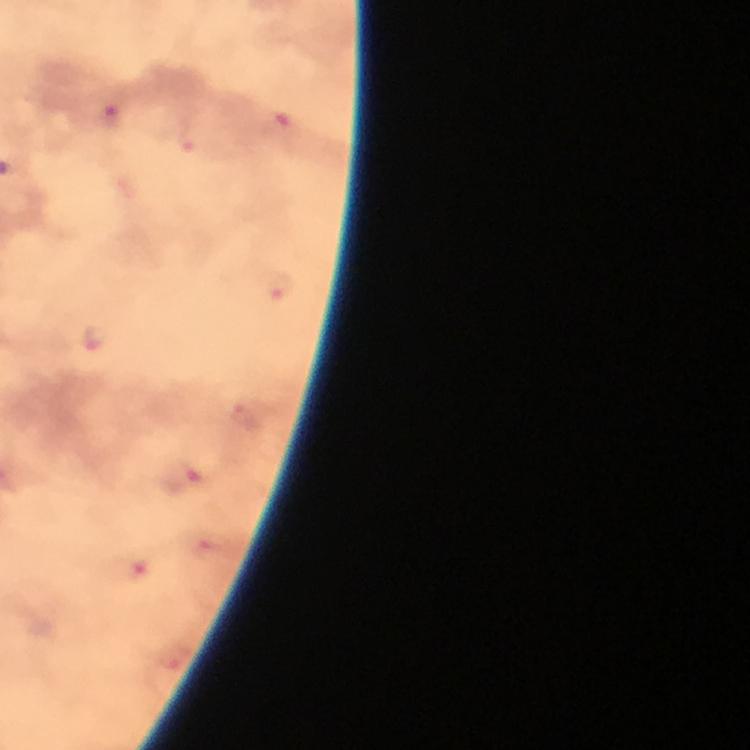
Approximate centers as (x, y) in pixels.
Summary:
  - Plasmodium parasite locations: (113, 114), (278, 125), (185, 139), (282, 286), (101, 339), (247, 417), (184, 476)
  - Context: from a diagnostic examination for malaria
  - Magnification: 100x
  - Stain: Giemsa
  - Cropped from: a single field of view
  - Preparation: thick blood smear
  - Capture: smartphone camera through the microscope
  - Image size: 750×750 pixels
  - Immersion oil: applied